Report the malaria status of this cell.
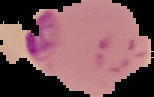

It is parasitized.

Summary:
  - Image type: segmented cell region on a black background
  - Preparation: thin blood smear
  - Image size: 154×97 pixels